Comment on the morphology of the red blood cells.
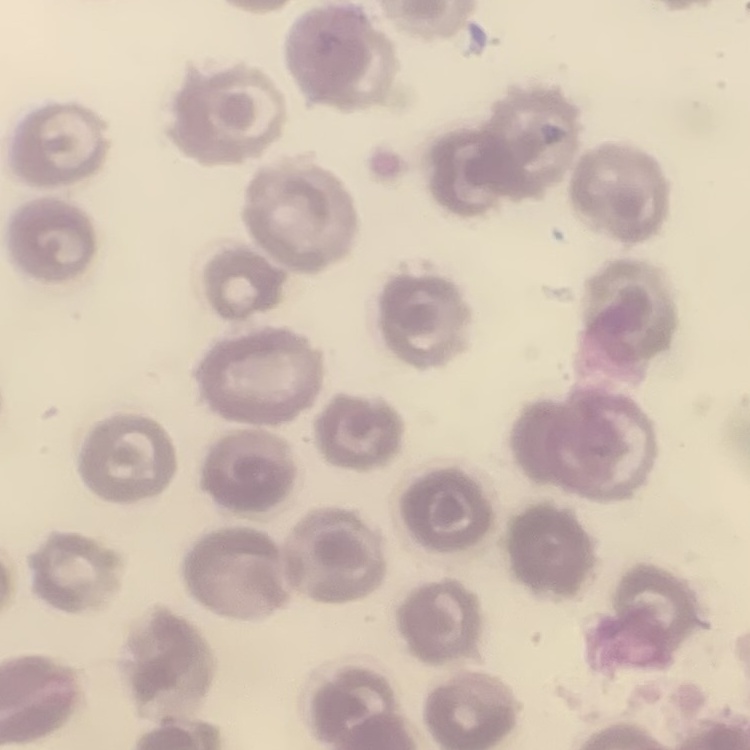

They show no rouleaux formation.

Summary:
  - Image type: one tile cut from a larger photomicrograph
  - Stain: Field's or Giemsa
  - Preparation: thin blood smear